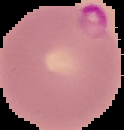

Summary:
  - Image type: cell region segmented out of the field of view; surrounding area masked to black
  - Preparation: thin blood film
  - Result: malaria parasites identified
  - Image size: 124×130 pixels